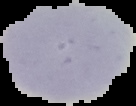
{
  "result": "negative for malaria parasites",
  "preparation": "thin blood smear",
  "image_type": "cell region segmented out of the field of view; surrounding area masked to black",
  "image_size": "136×106 pixels"
}